Locate every Plasmodium parasite.
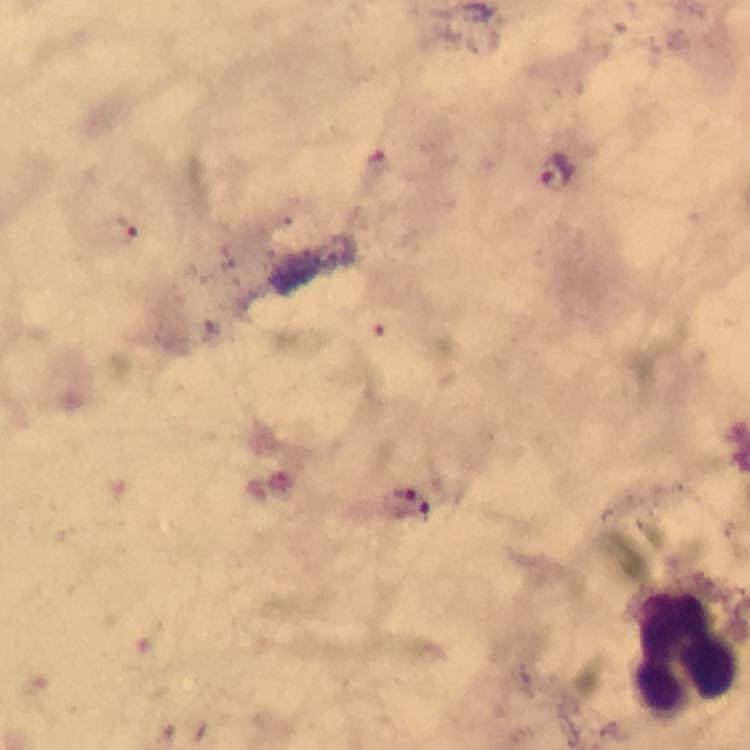
Approximate centers as [x, y] in pixels.
Plasmodium parasites: [552, 166], [125, 233].

Summary:
  - Leukocyte locations: [687, 652]
  - Context: from a diagnostic examination for malaria
  - Immersion oil: used
  - Cropped from: one field of view
  - Capture: smartphone mounted on the microscope
  - Stain: Giemsa
  - Image size: 750×750 pixels
  - Magnification: 100x
  - Preparation: thick blood film